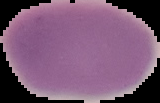

Summary:
  - Preparation: thin blood film
  - Malaria status: uninfected
  - Image type: segmented cell region with the area outside set to black
  - Image size: 160×103 pixels